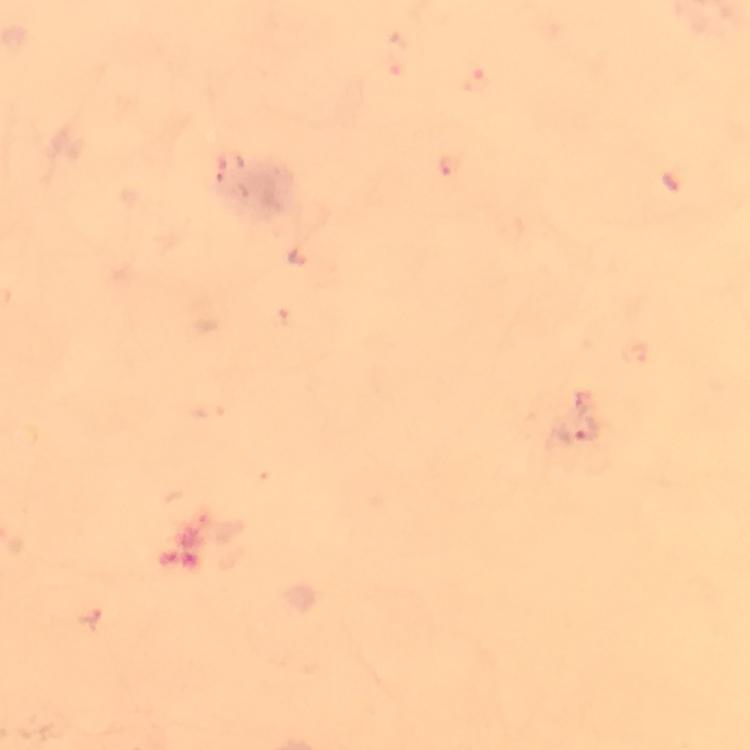

Approximate centers as [x, y] in pixels.
Summary:
  - Plasmodium parasite locations: [589, 432]
  - Magnification: 100x
  - Cropped from: a single field of view
  - Image size: 750×750 pixels
  - Preparation: thick blood film
  - Context: from a malaria diagnostic workup
  - Capture: smartphone photograph through a microscope
  - Immersion oil: used
  - Stain: Giemsa